Identify the parasite.
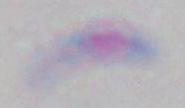
Toxoplasma gondii.

1000x magnification. Micrograph.